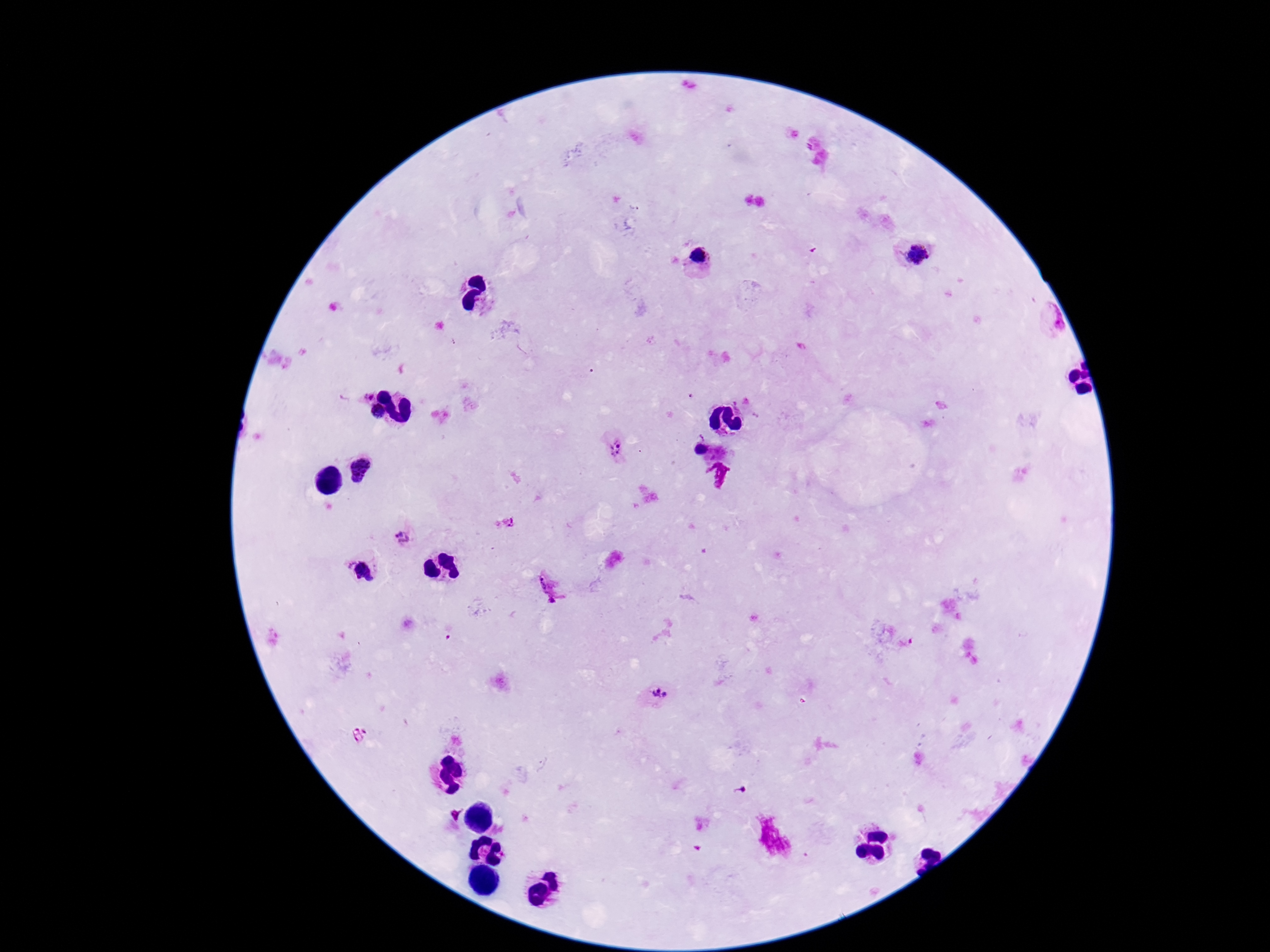
preparation = thick blood smear
field of view = one from this slide
capture = smartphone camera through the microscope eyepiece
patient malaria status = positive
magnification = 100x
image size = 1270×952 pixels
Plasmodium parasite locations = approximate object centers, in pixels from the top-left corner: (x=689, y=86), (x=792, y=133), (x=917, y=254), (x=699, y=255), (x=1050, y=320), (x=369, y=396), (x=378, y=411), (x=615, y=448), (x=701, y=450), (x=362, y=468), (x=506, y=526), (x=402, y=538), (x=363, y=572), (x=544, y=583), (x=552, y=599), (x=656, y=692), (x=666, y=695), (x=358, y=735)
stain = Giemsa